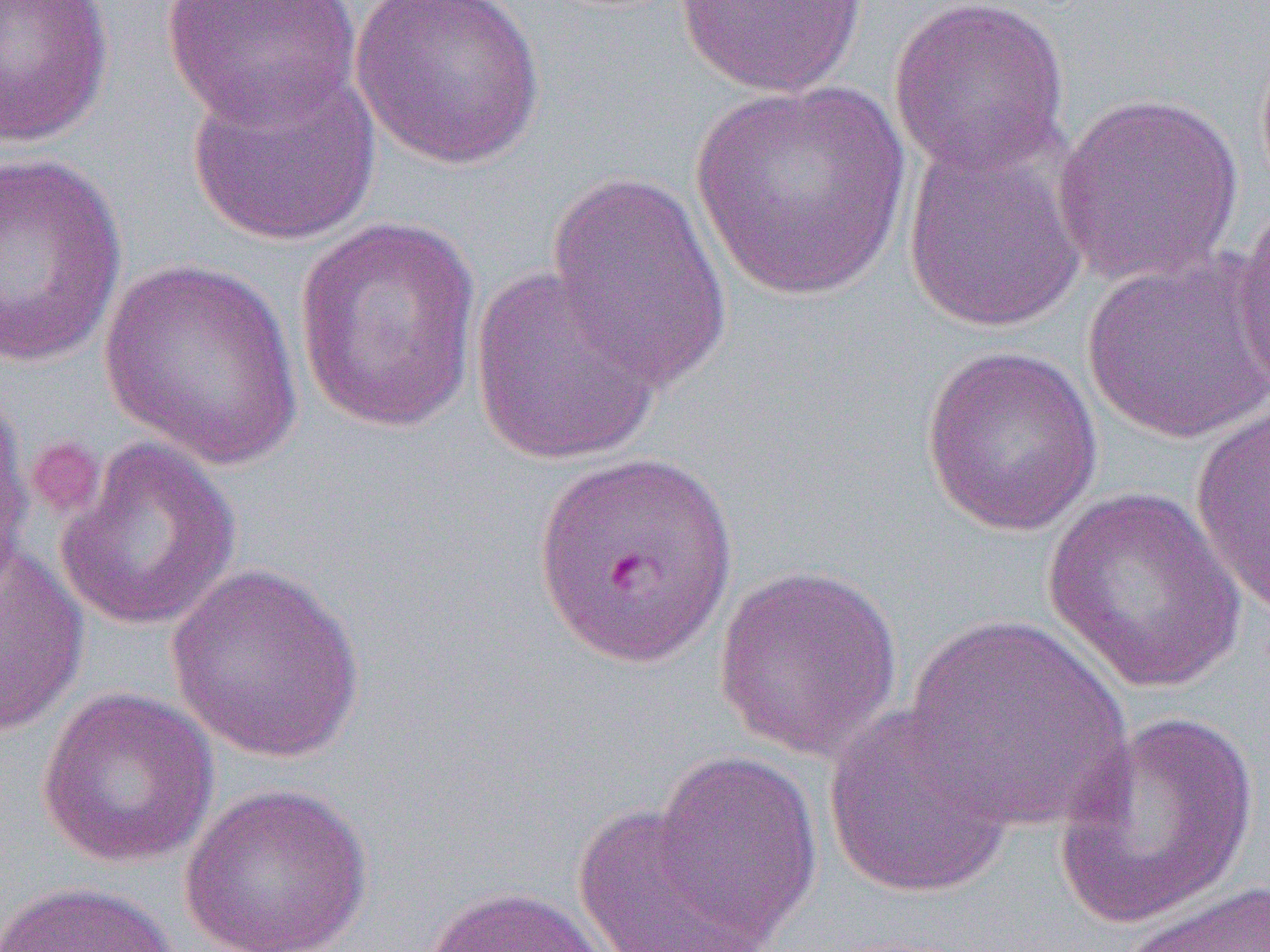
{
  "slide_level_diagnosis": "Plasmodium falciparum",
  "image_size": "1270×952 pixels",
  "field_of_view": "one of a larger specimen",
  "platelet_locations": "approximate bounding boxes as (x1, y1, x2, y2) in pixels: (24, 435, 106, 519)",
  "preparation": "thin blood smear",
  "modality": "light microscopy",
  "uninfected_red_blood_cell_locations": "approximate bounding boxes as (x1, y1, x2, y2) in pixels: (0, 0, 115, 148), (161, 0, 363, 128), (349, 0, 550, 171), (674, 0, 870, 98), (888, 0, 1071, 178), (184, 60, 381, 248), (687, 80, 916, 304), (1052, 91, 1244, 289), (902, 134, 1088, 333), (0, 150, 128, 372), (543, 169, 736, 391), (1233, 198, 1270, 404), (292, 216, 484, 435), (1081, 253, 1269, 444), (97, 258, 306, 469), (468, 264, 664, 465), (920, 343, 1104, 537), (0, 383, 36, 599), (1190, 403, 1269, 618), (54, 437, 242, 632), (533, 446, 740, 669), (1041, 487, 1252, 694), (0, 542, 89, 737), (165, 561, 368, 763), (712, 562, 906, 762), (904, 612, 1134, 831), (36, 686, 220, 869), (822, 702, 1018, 899), (1054, 713, 1259, 929), (651, 749, 824, 945), (178, 783, 375, 952), (570, 803, 775, 952), (1117, 879, 1270, 952), (0, 881, 181, 952), (417, 884, 618, 952)",
  "magnification": "1000x"
}